Outline each blood parasite and name the species.
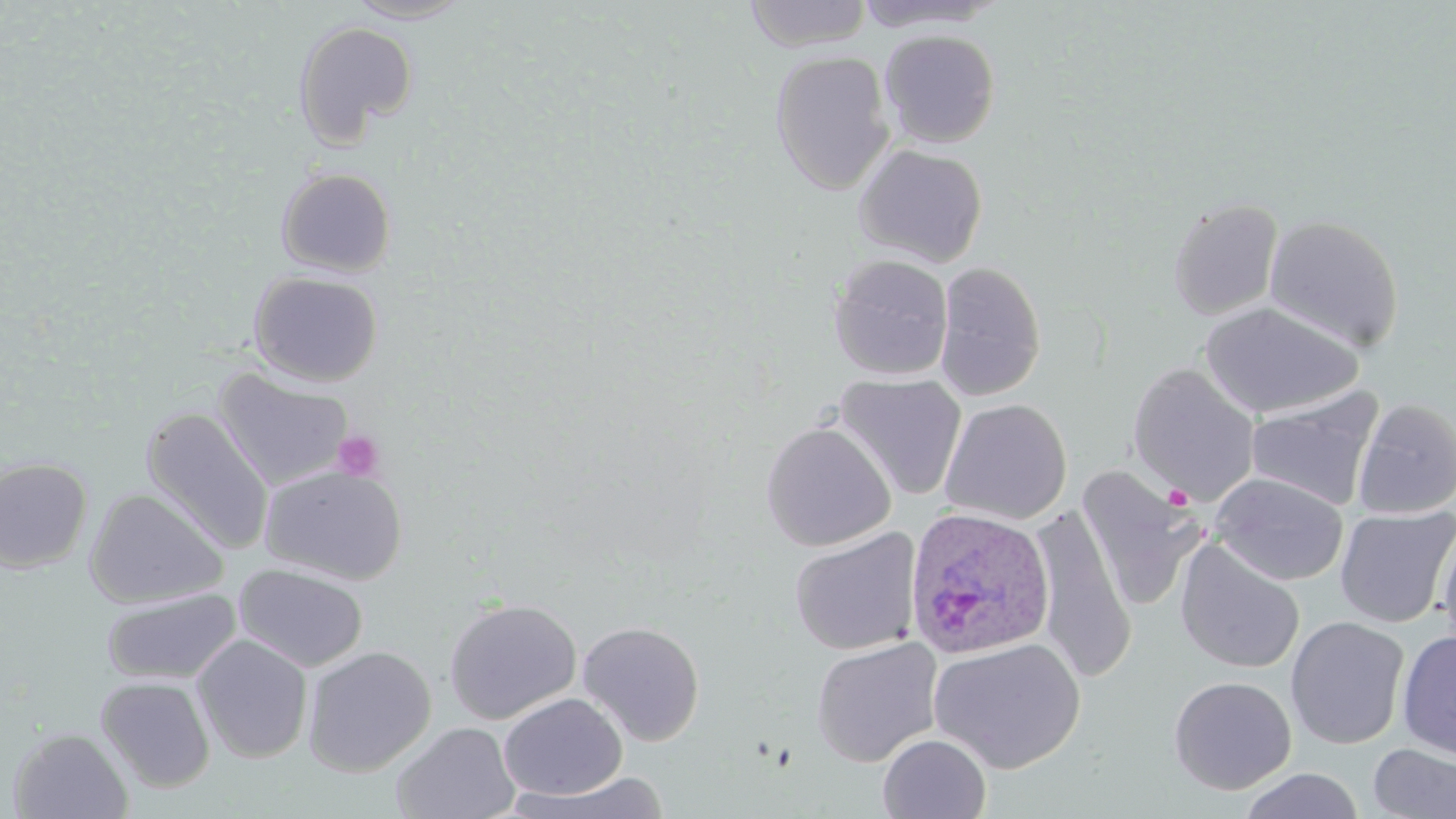

Approximate bounding boxes as [x1, y1, x2, y2] in pixels.
Plasmodium ovale-infected red blood cells: [903, 506, 1056, 660].
No Plasmodium falciparum, Plasmodium malariae, Plasmodium vivax, Babesia divergens, or Trypanosoma brucei observed.

{
  "slide_level_diagnosis": "Plasmodium ovale",
  "modality": "optical microscopy",
  "image_size": "1456×819 pixels",
  "magnification": "1000x",
  "platelet_locations": "approximate bounding boxes as [x1, y1, x2, y2] in pixels: [331, 430, 385, 481], [1163, 483, 1193, 509]",
  "uninfected_red_blood_cell_locations": "approximate bounding boxes as [x1, y1, x2, y2] in pixels: [345, 0, 471, 23], [743, 1, 873, 51], [293, 20, 418, 147], [879, 28, 1001, 149], [769, 50, 895, 194], [853, 143, 988, 267], [275, 167, 397, 277], [1167, 196, 1284, 320], [1264, 214, 1405, 353], [828, 254, 953, 381], [934, 261, 1047, 402], [248, 270, 384, 387], [1200, 301, 1362, 419], [1127, 363, 1261, 506], [213, 368, 354, 490], [834, 372, 967, 502], [1246, 389, 1385, 511], [1353, 397, 1456, 519], [939, 398, 1072, 524], [140, 407, 274, 555], [760, 421, 896, 552], [0, 457, 94, 573], [259, 463, 408, 585], [1076, 466, 1203, 613], [1210, 472, 1349, 587], [85, 487, 228, 609], [1027, 505, 1136, 683], [1334, 506, 1455, 629], [1435, 518, 1455, 658], [789, 528, 921, 656], [1174, 539, 1305, 675], [233, 563, 369, 673], [101, 587, 242, 685], [442, 597, 582, 725], [1285, 616, 1410, 749], [576, 621, 705, 746], [1397, 630, 1456, 761], [192, 634, 313, 763], [810, 636, 944, 767], [928, 638, 1087, 773], [302, 645, 436, 777], [96, 675, 216, 793], [1167, 675, 1297, 795], [498, 693, 628, 800], [391, 721, 520, 819], [6, 727, 134, 818], [877, 733, 991, 818], [1368, 743, 1456, 819], [1239, 768, 1365, 819], [508, 771, 670, 817]",
  "field_of_view": "one of a larger specimen",
  "preparation": "thin blood film",
  "stain": "May-Grünwald-Giemsa"
}